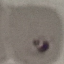 Malaria status: parasitized. Automatically extracted cell patch, resized to 64 × 64 pixels. Thin smear of blood. Photographed with a smartphone camera at the microscope eyepiece. Giemsa-stained preparation.